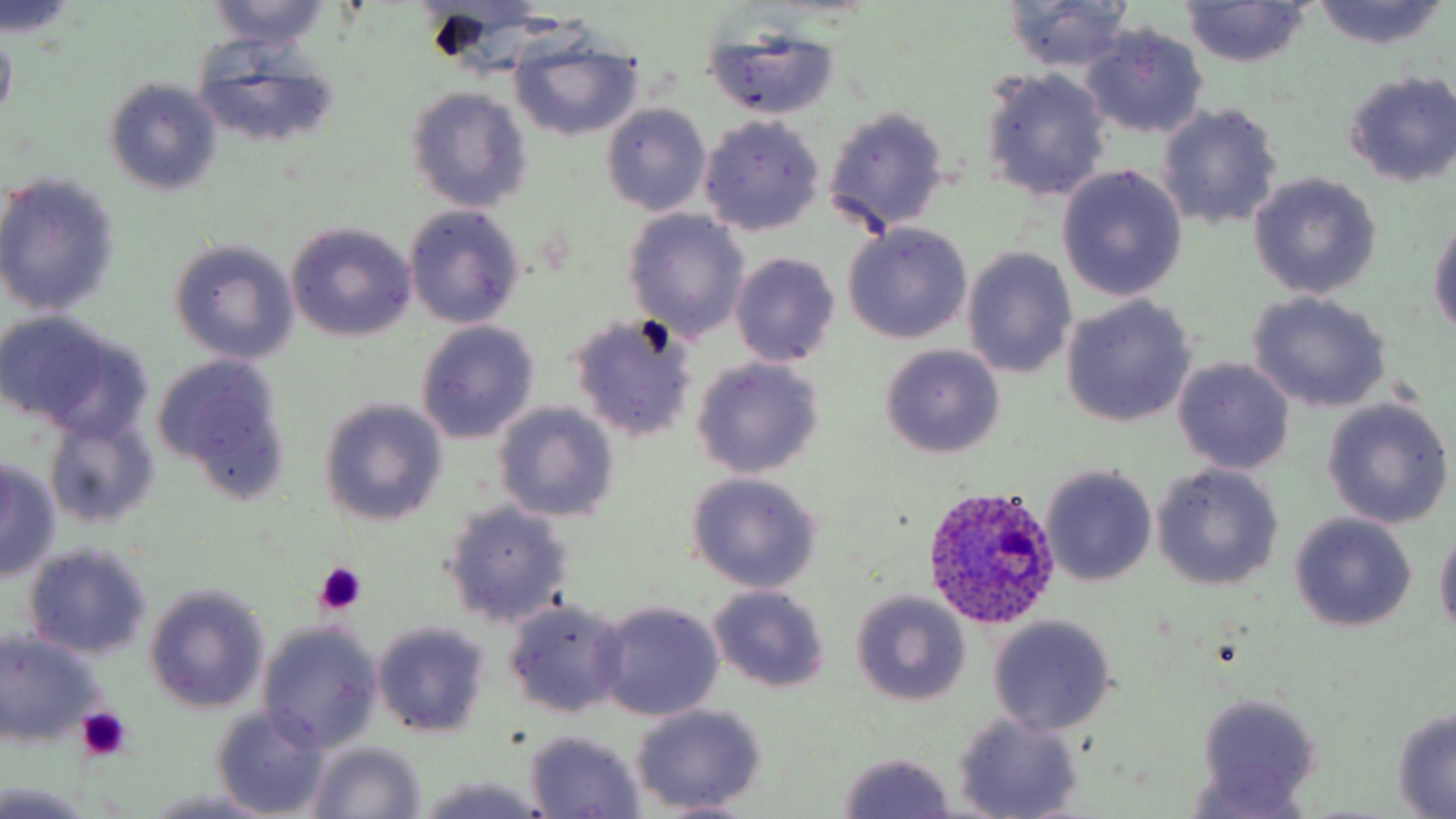

Summary:
  - Coordinate format: approximate bounding boxes as [x1, y1, x2, y2] in pixels
  - Platelet locations: [313, 564, 367, 616], [75, 707, 132, 761]
  - Plasmodium ovale-infected red blood cell locations: [921, 484, 1063, 630]
  - Uninfected red blood cell locations: [203, 0, 331, 49], [1309, 0, 1450, 50], [0, 2, 82, 42], [1001, 2, 1137, 73], [1179, 2, 1311, 68], [0, 21, 17, 125], [1080, 22, 1209, 140], [700, 24, 842, 121], [508, 30, 645, 143], [188, 40, 342, 152], [981, 68, 1111, 202], [1341, 69, 1455, 189], [104, 79, 223, 196], [405, 87, 534, 214], [1157, 101, 1284, 232], [603, 103, 710, 216], [823, 106, 950, 236], [698, 116, 826, 236], [1056, 165, 1188, 302], [1249, 173, 1381, 299], [0, 174, 123, 316], [404, 205, 527, 331], [623, 209, 751, 341], [1427, 213, 1456, 338], [285, 222, 418, 343], [842, 224, 972, 344], [168, 238, 300, 363], [961, 247, 1079, 380], [730, 253, 841, 368], [1247, 290, 1391, 413], [1061, 295, 1197, 429], [566, 311, 700, 443], [0, 314, 142, 433], [415, 322, 539, 443], [878, 344, 1005, 460], [152, 355, 292, 503], [692, 357, 825, 479], [1172, 358, 1294, 475], [319, 399, 448, 526], [1323, 399, 1453, 529], [495, 402, 620, 523], [42, 412, 161, 531], [0, 459, 61, 582], [1040, 463, 1157, 588], [1154, 463, 1283, 590], [685, 472, 824, 592], [440, 500, 575, 629], [1288, 513, 1416, 634], [1433, 526, 1456, 640], [21, 543, 153, 660], [144, 584, 272, 715], [707, 585, 831, 692], [851, 590, 971, 707], [501, 598, 630, 719], [593, 600, 726, 723], [987, 615, 1117, 735], [256, 622, 382, 753], [372, 622, 490, 739], [0, 631, 105, 746], [1194, 693, 1324, 813], [630, 705, 767, 816], [1389, 705, 1456, 816], [211, 706, 332, 817], [951, 711, 1085, 819], [525, 731, 646, 816], [305, 741, 427, 819], [834, 752, 959, 819], [417, 777, 549, 818], [0, 781, 96, 818], [147, 786, 276, 819], [644, 797, 763, 816]
  - Slide-level diagnosis: Plasmodium ovale
  - Modality: light microscopy
  - Field of view: one of a larger specimen
  - Magnification: 1000x
  - Preparation: thin blood smear
  - Stain: May-Grünwald-Giemsa
  - Image size: 1456×819 pixels